Locate every malaria parasite and every leukocyte.
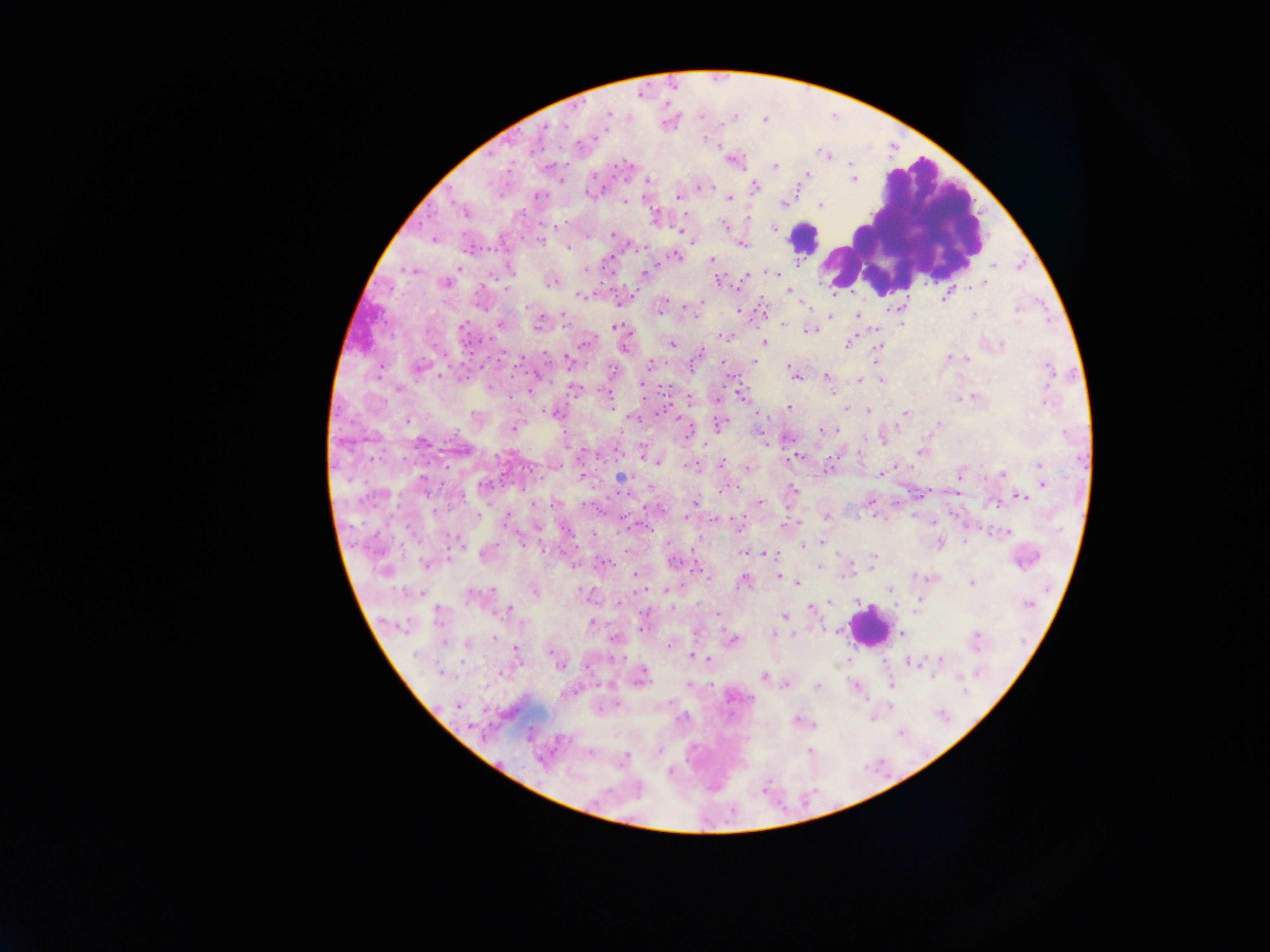
Approximate centers as x y in pixels.
Malaria parasites: 607 114; 765 119; 605 131; 703 139; 717 145; 733 160; 851 162; 775 166; 806 174; 560 180; 647 180; 853 180; 698 187; 753 187; 588 194; 536 195; 678 196; 729 198; 623 201; 781 202; 820 203; 464 211; 654 218; 555 225; 774 226; 725 227; 773 228; 681 230; 586 235; 612 235; 433 239; 540 241; 741 243; 568 247; 645 248; 674 255; 711 260; 993 266; 413 270; 584 270; 770 272; 646 273; 747 277; 718 280; 553 281; 445 282; 985 282; 982 285; 504 287; 788 291; 946 294; 580 296; 621 300; 805 304; 662 305; 762 310; 738 311; 972 314; 562 315; 857 315; 830 316; 500 323; 901 323; 538 324; 783 324; 616 327; 809 330; 723 335; 849 341; 584 343; 670 343; 764 343; 1001 345; 623 346; 877 348; 698 354; 949 357; 875 358; 967 359; 568 361; 754 362; 651 364; 723 365; 419 367; 482 368; 789 368; 797 375; 536 376; 825 376; 732 377; 881 380; 859 381; 643 383; 398 388; 573 389; 529 391; 741 395; 607 397; 973 397; 716 399; 1045 401; 788 407; 845 409; 868 411; 553 412; 905 414; 632 417; 719 425; 939 426; 513 429; 821 430; 760 433; 863 440; 421 442; 643 452; 921 452; 796 456; 658 460; 721 463; 896 464; 1040 464; 689 466; 746 468; 827 469; 880 473; 1002 473; 960 474; 581 476; 621 477; 1043 484; 484 485; 650 488; 792 489; 928 491; 1021 497; 695 502; 759 502; 868 502; 994 503; 506 516; 826 517; 622 518; 686 519; 714 519; 882 519; 734 521; 799 523; 647 528; 567 530; 1007 531; 592 534; 519 540; 964 542; 822 543; 940 543; 804 545; 745 552; 486 553; 768 553; 872 561; 426 563; 603 564; 573 566; 819 567; 635 574; 778 576; 932 576; 743 580; 797 582; 971 582; 533 589; 666 589; 644 590; 891 590; 419 593; 474 595; 587 596; 830 602; 811 608; 508 609; 915 611; 439 613; 717 614; 783 616; 592 622; 402 626; 641 629; 900 633; 772 634; 615 638; 731 640; 467 644; 668 644; 515 649; 551 653; 416 655; 694 656; 709 660; 940 660; 910 662; 559 664; 441 673; 502 673; 641 676; 958 676; 763 677; 786 684; 891 685; 687 686; 817 687; 855 687; 616 704; 457 705; 797 721; 658 751; 810 751; 590 753; 621 760; 670 773.
Leukocytes: 903 227; 803 237; 867 626.

field of view = single
country = Ghana
image size = 1270×952 pixels
preparation = thick blood smear
capture = mobile-phone photograph through a microscope